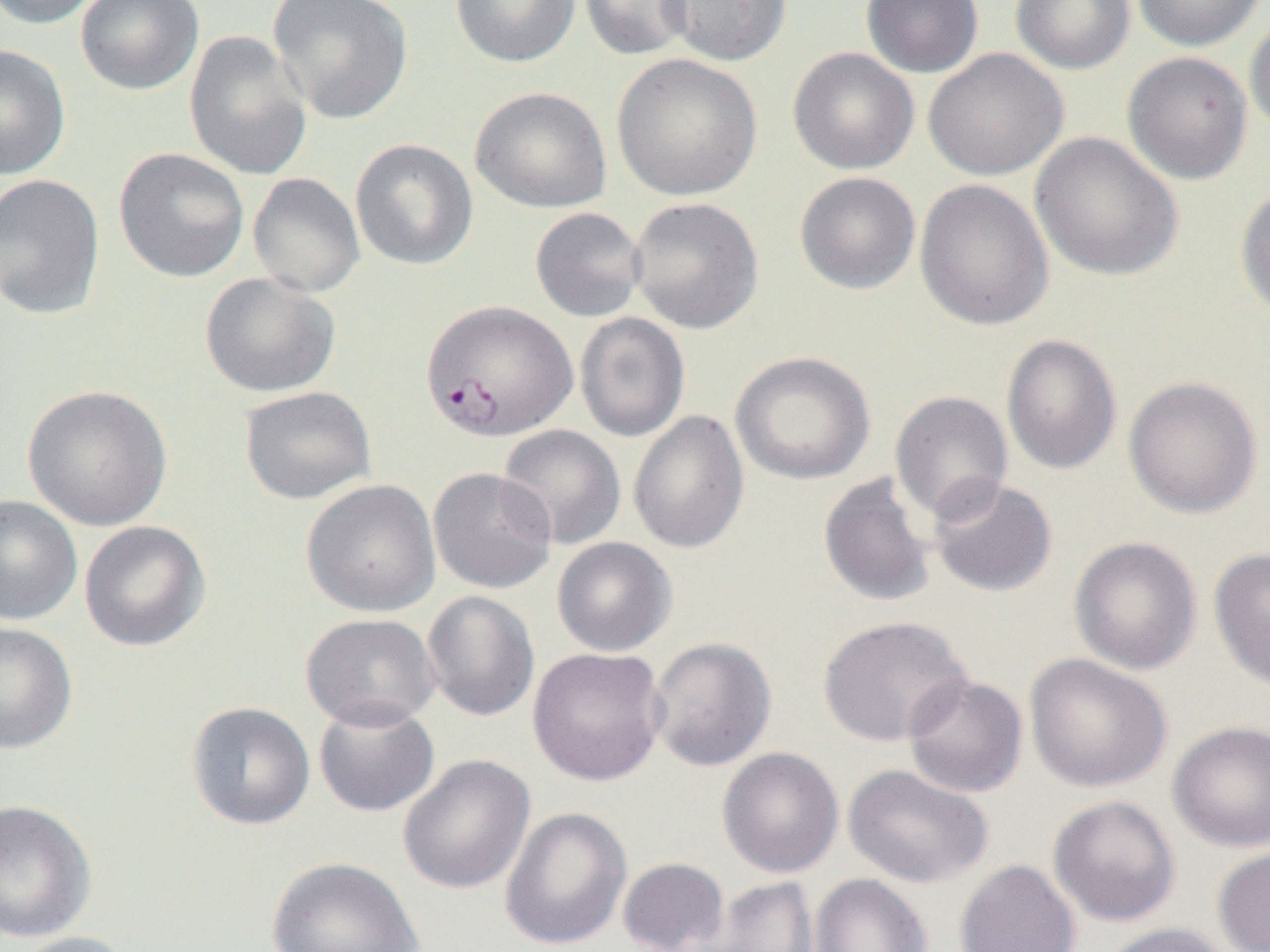

slide_level_diagnosis: Plasmodium falciparum
field_of_view: one of a larger specimen
preparation: thin blood smear
magnification: 1000x
plasmodium_falciparum_infected_red_blood_cell_locations: 'approximate bounding boxes as named x1/y1/x2/y2 corners in pixels: (x1=421, y1=299, x2=577, y2=442)'
image_size: 1270×952 pixels
modality: optical microscopy
uninfected_red_blood_cell_locations: 'approximate bounding boxes as named x1/y1/x2/y2 corners in pixels: (x1=1, y1=0, x2=107, y2=30), (x1=75, y1=0, x2=205, y2=95), (x1=267, y1=0, x2=413, y2=125), (x1=450, y1=0, x2=581, y2=68), (x1=580, y1=0, x2=694, y2=60), (x1=661, y1=0, x2=793, y2=66), (x1=861, y1=0, x2=984, y2=78), (x1=1011, y1=0, x2=1136, y2=74), (x1=1131, y1=0, x2=1266, y2=51), (x1=1245, y1=13, x2=1270, y2=141), (x1=184, y1=30, x2=312, y2=182), (x1=0, y1=44, x2=71, y2=180), (x1=788, y1=47, x2=919, y2=175), (x1=923, y1=48, x2=1068, y2=181), (x1=1122, y1=51, x2=1253, y2=185), (x1=611, y1=53, x2=762, y2=201), (x1=470, y1=86, x2=612, y2=214), (x1=1030, y1=132, x2=1183, y2=282), (x1=350, y1=139, x2=479, y2=271), (x1=113, y1=147, x2=250, y2=283), (x1=794, y1=172, x2=921, y2=294), (x1=0, y1=173, x2=106, y2=320), (x1=247, y1=173, x2=365, y2=297), (x1=914, y1=179, x2=1054, y2=331), (x1=1235, y1=185, x2=1270, y2=321), (x1=628, y1=197, x2=764, y2=334), (x1=530, y1=207, x2=647, y2=322), (x1=199, y1=272, x2=340, y2=398), (x1=574, y1=312, x2=690, y2=442), (x1=1001, y1=333, x2=1122, y2=475), (x1=730, y1=351, x2=876, y2=485), (x1=1123, y1=376, x2=1263, y2=519), (x1=22, y1=384, x2=173, y2=531), (x1=239, y1=386, x2=376, y2=505), (x1=889, y1=391, x2=1014, y2=524), (x1=628, y1=410, x2=749, y2=553), (x1=497, y1=425, x2=626, y2=550), (x1=428, y1=467, x2=557, y2=593), (x1=818, y1=471, x2=937, y2=608), (x1=927, y1=476, x2=1058, y2=597), (x1=301, y1=479, x2=441, y2=618), (x1=0, y1=494, x2=83, y2=626), (x1=79, y1=520, x2=212, y2=651), (x1=1068, y1=536, x2=1202, y2=675), (x1=551, y1=537, x2=677, y2=656), (x1=1209, y1=547, x2=1270, y2=690), (x1=421, y1=590, x2=540, y2=722), (x1=300, y1=613, x2=441, y2=731), (x1=817, y1=615, x2=972, y2=747), (x1=0, y1=622, x2=78, y2=753), (x1=646, y1=636, x2=777, y2=771), (x1=527, y1=646, x2=668, y2=786), (x1=1024, y1=653, x2=1172, y2=793), (x1=902, y1=674, x2=1028, y2=798), (x1=313, y1=699, x2=440, y2=817), (x1=185, y1=701, x2=316, y2=830), (x1=1167, y1=720, x2=1270, y2=852), (x1=717, y1=747, x2=844, y2=878), (x1=398, y1=754, x2=535, y2=894), (x1=843, y1=764, x2=993, y2=889), (x1=1047, y1=795, x2=1181, y2=927), (x1=0, y1=799, x2=97, y2=942), (x1=500, y1=806, x2=632, y2=950), (x1=1212, y1=845, x2=1270, y2=952), (x1=267, y1=856, x2=424, y2=952), (x1=617, y1=857, x2=730, y2=952), (x1=955, y1=859, x2=1081, y2=952), (x1=808, y1=873, x2=933, y2=952), (x1=704, y1=876, x2=819, y2=952), (x1=1098, y1=922, x2=1236, y2=952), (x1=8, y1=931, x2=140, y2=952)'